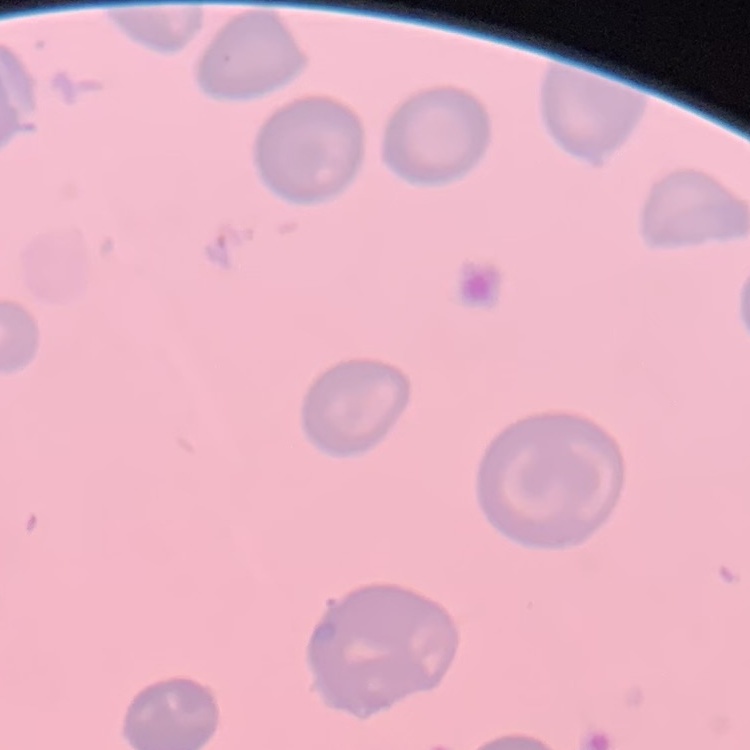 The red blood cells exhibit no rouleaux formation. Field's or Giemsa stain. Thin peripheral smear. Square crop of a larger photomicrograph.